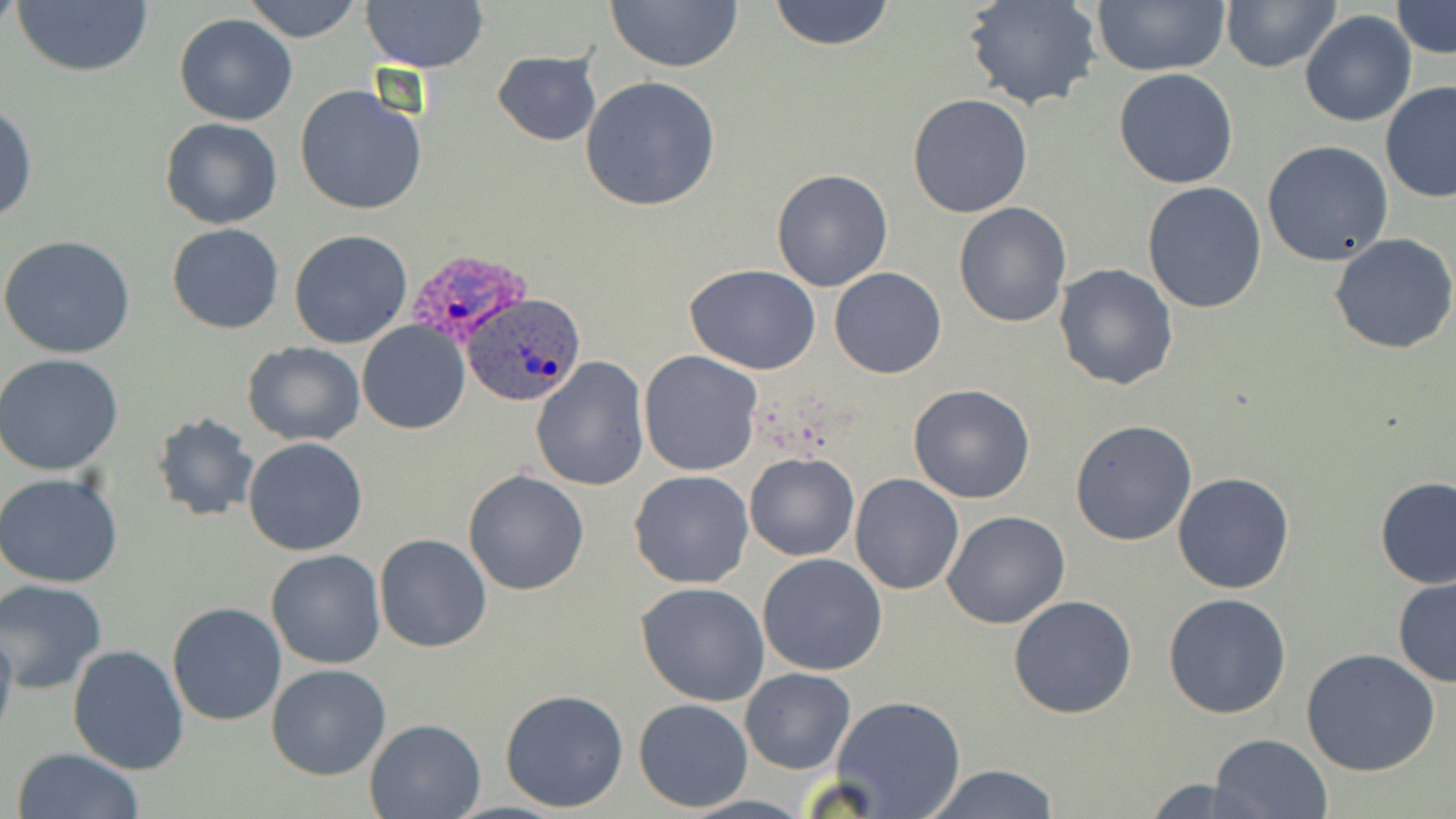 Approximate bounding boxes as named x1/y1/x2/y2 corners in pixels. Uninfected red blood cell locations: (x1=11, y1=0, x2=154, y2=79), (x1=242, y1=0, x2=366, y2=43), (x1=768, y1=0, x2=895, y2=51), (x1=1090, y1=0, x2=1230, y2=75), (x1=1220, y1=0, x2=1339, y2=73), (x1=362, y1=1, x2=489, y2=73), (x1=605, y1=1, x2=744, y2=74), (x1=965, y1=1, x2=1101, y2=111), (x1=1392, y1=2, x2=1455, y2=57), (x1=1300, y1=11, x2=1416, y2=127), (x1=174, y1=13, x2=298, y2=125), (x1=493, y1=49, x2=601, y2=146), (x1=1114, y1=68, x2=1238, y2=188), (x1=581, y1=76, x2=721, y2=213), (x1=1378, y1=82, x2=1456, y2=202), (x1=294, y1=84, x2=429, y2=216), (x1=907, y1=94, x2=1033, y2=217), (x1=0, y1=102, x2=37, y2=227), (x1=159, y1=117, x2=283, y2=230), (x1=1262, y1=140, x2=1393, y2=267), (x1=770, y1=169, x2=894, y2=292), (x1=1142, y1=182, x2=1268, y2=315), (x1=953, y1=202, x2=1073, y2=327), (x1=166, y1=223, x2=285, y2=334), (x1=289, y1=228, x2=414, y2=349), (x1=1328, y1=232, x2=1456, y2=355), (x1=1, y1=234, x2=135, y2=358), (x1=1053, y1=262, x2=1179, y2=390), (x1=683, y1=264, x2=822, y2=376), (x1=830, y1=266, x2=946, y2=379), (x1=357, y1=321, x2=470, y2=434), (x1=242, y1=343, x2=366, y2=445), (x1=639, y1=351, x2=764, y2=477), (x1=0, y1=354, x2=125, y2=475), (x1=530, y1=357, x2=650, y2=490), (x1=907, y1=383, x2=1035, y2=504), (x1=151, y1=413, x2=258, y2=523), (x1=1070, y1=419, x2=1197, y2=546), (x1=243, y1=437, x2=369, y2=556), (x1=744, y1=451, x2=859, y2=561), (x1=463, y1=469, x2=590, y2=595), (x1=628, y1=470, x2=754, y2=589), (x1=0, y1=471, x2=124, y2=587), (x1=1171, y1=472, x2=1294, y2=594), (x1=849, y1=473, x2=964, y2=594), (x1=1374, y1=475, x2=1456, y2=589), (x1=942, y1=511, x2=1071, y2=629), (x1=373, y1=534, x2=492, y2=654), (x1=265, y1=549, x2=386, y2=670), (x1=757, y1=554, x2=889, y2=676), (x1=1392, y1=576, x2=1456, y2=687), (x1=0, y1=580, x2=110, y2=694), (x1=637, y1=581, x2=770, y2=705), (x1=1163, y1=593, x2=1292, y2=718), (x1=1008, y1=595, x2=1137, y2=719), (x1=167, y1=601, x2=288, y2=725), (x1=0, y1=613, x2=18, y2=751), (x1=67, y1=643, x2=191, y2=774), (x1=1300, y1=647, x2=1441, y2=776), (x1=266, y1=663, x2=393, y2=781), (x1=739, y1=667, x2=855, y2=775), (x1=500, y1=687, x2=630, y2=813), (x1=831, y1=695, x2=968, y2=818), (x1=634, y1=698, x2=753, y2=813), (x1=364, y1=717, x2=486, y2=819), (x1=1209, y1=733, x2=1334, y2=819), (x1=10, y1=747, x2=146, y2=819), (x1=919, y1=763, x2=1061, y2=819), (x1=1140, y1=775, x2=1270, y2=818). Plasmodium ovale-infected red blood cell locations: (x1=404, y1=252, x2=532, y2=342), (x1=461, y1=292, x2=589, y2=408). Slide-level diagnosis: Plasmodium ovale. Light microscopy. May-Grünwald-Giemsa-stained preparation. Thin blood film. Image is 1456×819 pixels. Captured at 1000x magnification. Single field of view.